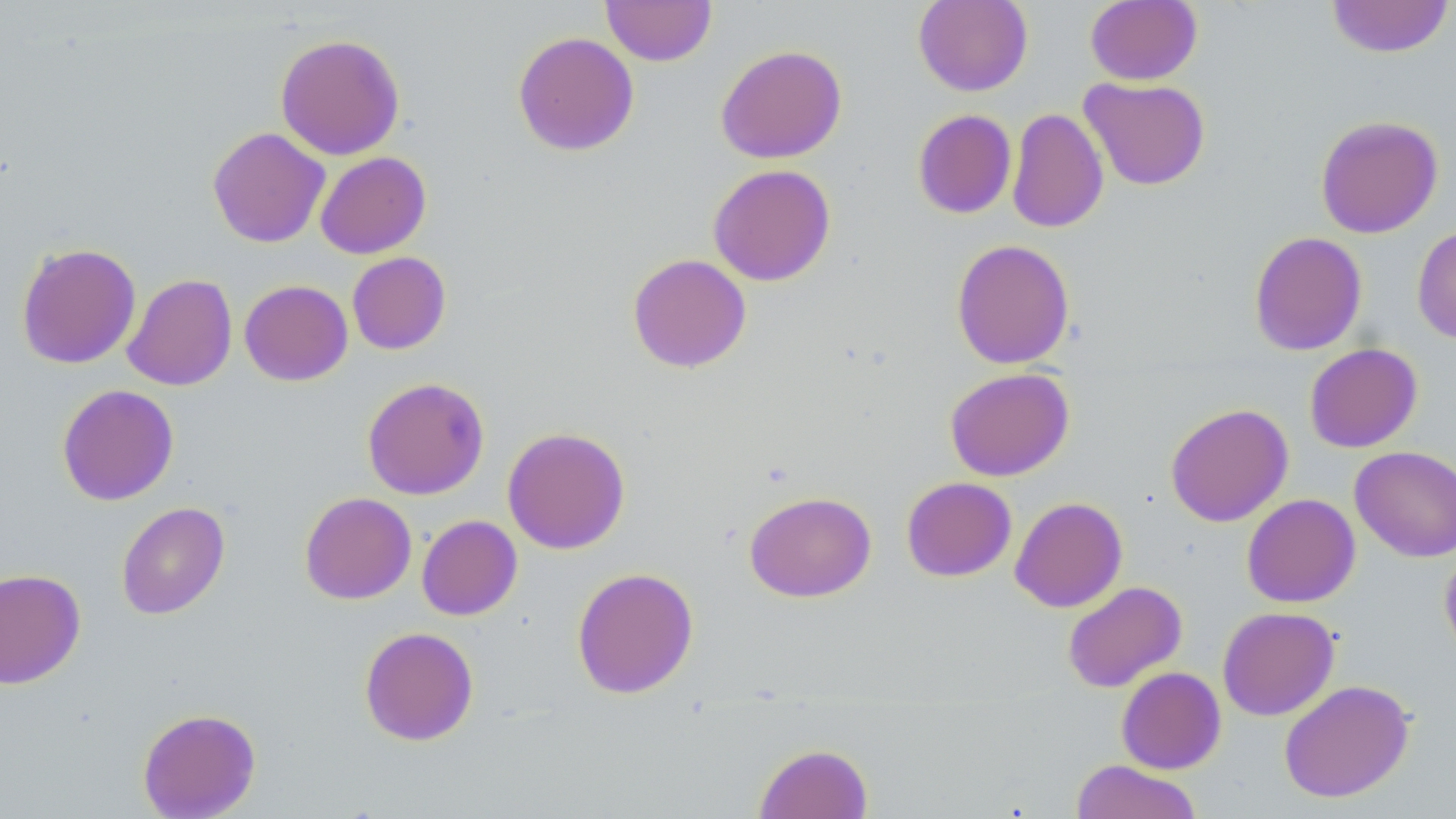
Summary:
  - Coordinate format: approximate bounding boxes as (x1, y1, x2, y2) in pixels
  - Uninfected red blood cell locations: (600, 0, 717, 66), (913, 0, 1033, 96), (1085, 0, 1202, 85), (1325, 0, 1454, 58), (512, 31, 639, 156), (275, 33, 405, 161), (715, 44, 847, 164), (1079, 77, 1211, 190), (1007, 107, 1109, 233), (912, 109, 1016, 219), (1315, 114, 1443, 238), (207, 126, 330, 247), (315, 151, 431, 259), (707, 164, 836, 287), (1412, 225, 1456, 344), (1249, 231, 1367, 355), (951, 239, 1075, 369), (16, 242, 141, 369), (347, 252, 451, 355), (627, 253, 751, 373), (122, 273, 237, 391), (239, 280, 353, 386), (1304, 343, 1423, 453), (944, 367, 1074, 481), (362, 376, 490, 500), (56, 384, 179, 506), (1166, 403, 1293, 527), (502, 426, 631, 555), (1350, 446, 1456, 562), (901, 476, 1017, 582), (744, 491, 876, 602), (299, 492, 416, 604), (1241, 493, 1360, 608), (1010, 496, 1128, 613), (116, 501, 230, 620), (417, 515, 522, 620), (1439, 545, 1456, 661), (571, 567, 699, 699), (0, 569, 85, 689), (1062, 581, 1187, 693), (1217, 606, 1340, 721), (359, 626, 479, 746), (1116, 667, 1226, 774), (1278, 679, 1415, 803), (137, 708, 261, 818), (754, 742, 873, 819), (1070, 760, 1203, 819)
  - Slide-level diagnosis: negative for blood parasites
  - Modality: light microscopy
  - Preparation: thin blood film
  - Image size: 1456×819 pixels
  - Magnification: 1000x
  - Field of view: single
  - Stain: May-Grünwald-Giemsa